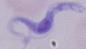 Photomicrograph. 1000x magnification. A trypanosome is shown.